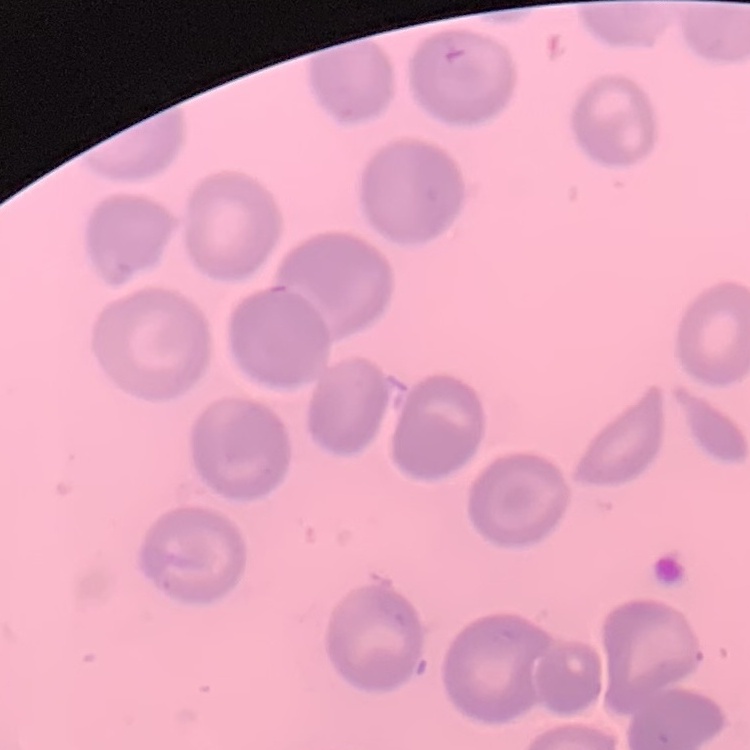 The red blood cells show no rouleaux formation. One tile cut from a larger photomicrograph. Thin blood smear. Stained with either Field's or Giemsa.